Name the parasite shown.
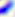
This is Toxoplasma gondii.

Summary:
  - Modality: micrograph
  - Magnification: 400x